Assess this cell for malaria.
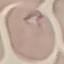
Parasitized.

Summary:
  - Preparation: thin smear
  - Capture: smartphone camera at the microscope eyepiece
  - Stain: Giemsa
  - Image type: cell patch, automatically extracted from a larger field of view and resized to 64 × 64 pixels